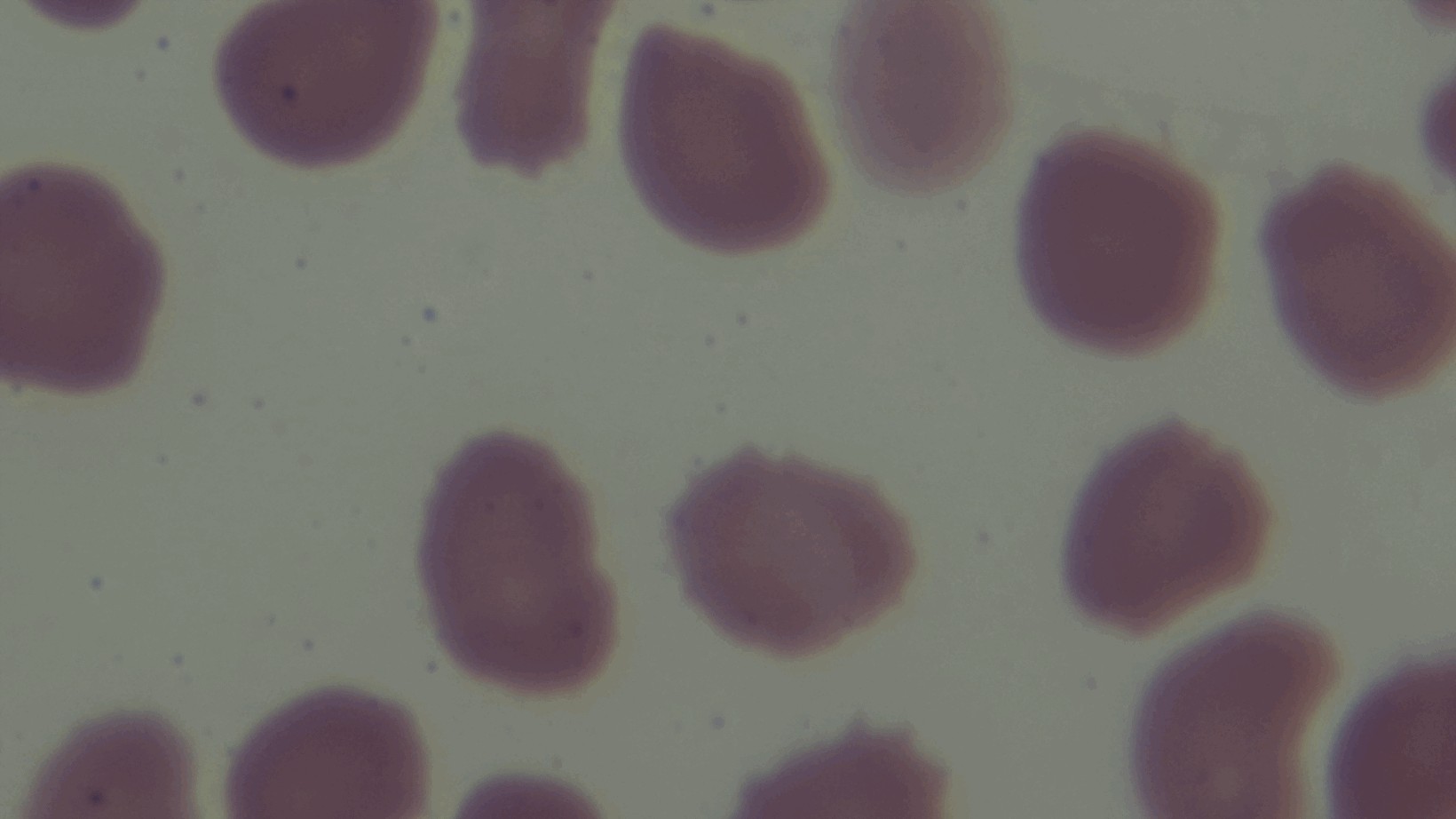

field of view = one from the slide
modality = light microscopy
capture = mounted 4K digital camera
objective = 100x oil immersion
preparation = thin smear
stain = Giemsa
malaria status = uninfected